Report the malaria status of this cell.
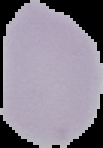
It is uninfected.

image size = 103×148 pixels
preparation = thin blood smear
image type = cell region segmented out of the field of view; surrounding area masked to black